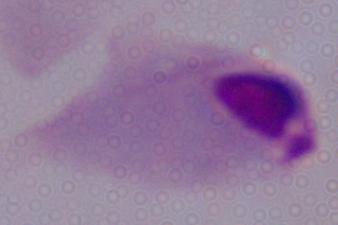

modality = photomicrograph
magnification = 1000x
identification = trichomonad